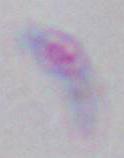

1000x magnification. Toxoplasma gondii is shown. Photomicrograph.